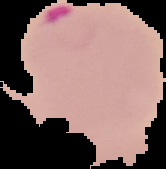

malaria_status: parasitized
image_type: segmented cell region with the area outside set to black
image_size: 166×169 pixels
preparation: thin blood film